Identify the parasite.
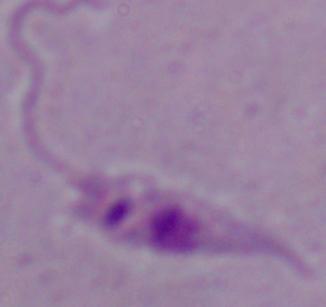
This is Leishmania.

Summary:
  - Modality: micrograph
  - Magnification: 1000x